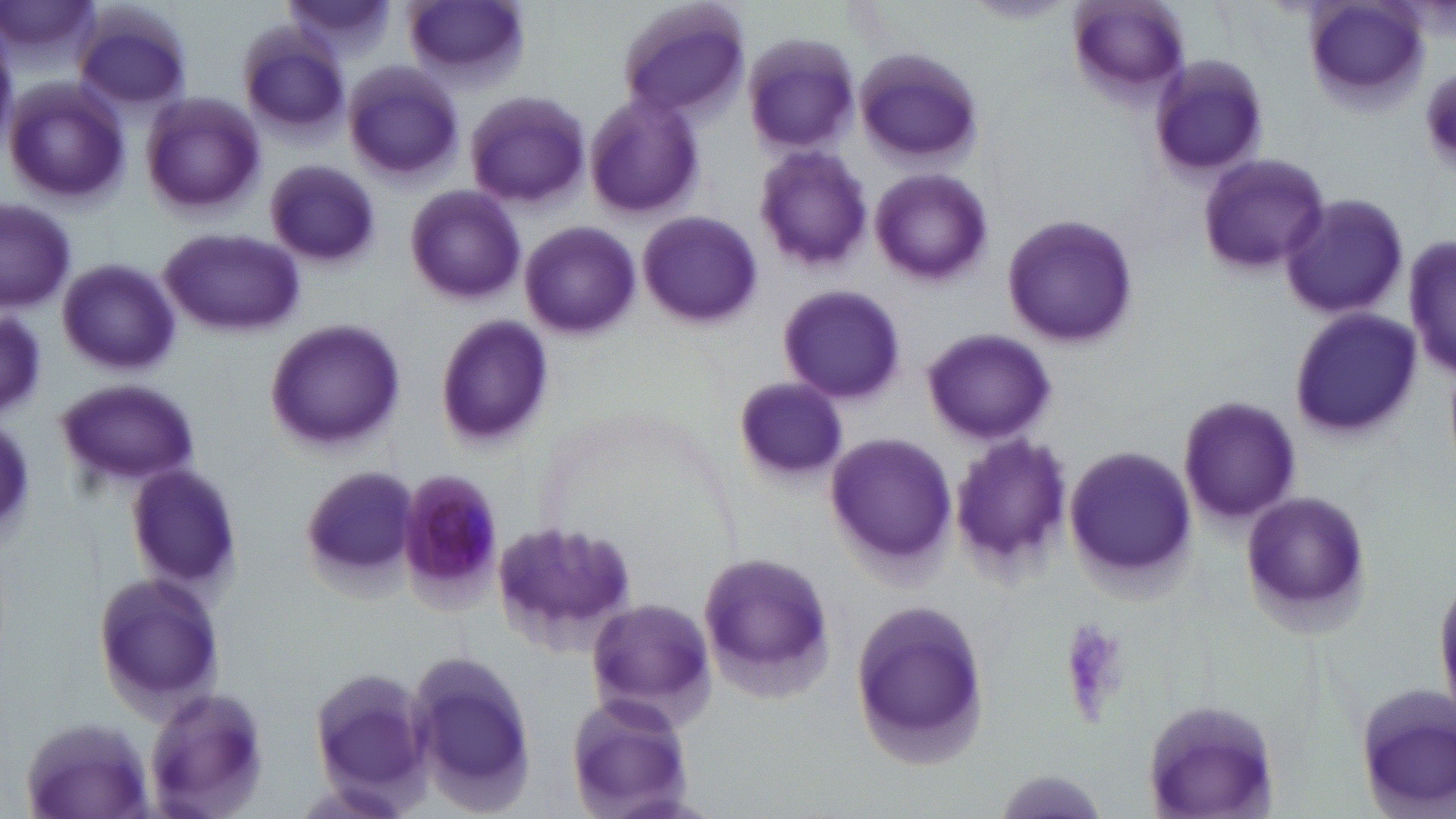 Approximate bounding boxes as named x1/y1/x2/y2 corners in pixels. Uninfected red blood cell locations: (x1=283, y1=0, x2=394, y2=60), (x1=404, y1=0, x2=526, y2=93), (x1=614, y1=0, x2=753, y2=121), (x1=967, y1=1, x2=1070, y2=24), (x1=1064, y1=1, x2=1193, y2=109), (x1=1299, y1=2, x2=1430, y2=113), (x1=74, y1=6, x2=192, y2=114), (x1=237, y1=24, x2=352, y2=139), (x1=741, y1=33, x2=863, y2=157), (x1=851, y1=46, x2=985, y2=169), (x1=1146, y1=54, x2=1270, y2=183), (x1=343, y1=63, x2=464, y2=183), (x1=5, y1=78, x2=130, y2=206), (x1=584, y1=89, x2=704, y2=221), (x1=463, y1=90, x2=591, y2=212), (x1=141, y1=91, x2=265, y2=218), (x1=751, y1=145, x2=874, y2=273), (x1=1196, y1=153, x2=1333, y2=279), (x1=266, y1=159, x2=379, y2=269), (x1=870, y1=169, x2=993, y2=286), (x1=404, y1=182, x2=524, y2=305), (x1=1276, y1=195, x2=1411, y2=320), (x1=1, y1=198, x2=76, y2=312), (x1=636, y1=211, x2=763, y2=330), (x1=1001, y1=212, x2=1138, y2=351), (x1=518, y1=220, x2=643, y2=341), (x1=160, y1=228, x2=304, y2=338), (x1=1408, y1=229, x2=1455, y2=384), (x1=57, y1=260, x2=181, y2=375), (x1=777, y1=286, x2=906, y2=406), (x1=1285, y1=308, x2=1423, y2=443), (x1=1, y1=309, x2=48, y2=413), (x1=435, y1=317, x2=554, y2=449), (x1=265, y1=318, x2=406, y2=452), (x1=921, y1=327, x2=1056, y2=445), (x1=58, y1=379, x2=203, y2=492), (x1=731, y1=379, x2=849, y2=481), (x1=1177, y1=393, x2=1302, y2=524), (x1=0, y1=411, x2=34, y2=544), (x1=825, y1=431, x2=955, y2=574), (x1=946, y1=433, x2=1072, y2=580), (x1=1064, y1=442, x2=1199, y2=589), (x1=125, y1=464, x2=246, y2=590), (x1=1237, y1=491, x2=1374, y2=634), (x1=490, y1=512, x2=639, y2=652), (x1=699, y1=548, x2=836, y2=699), (x1=91, y1=568, x2=226, y2=713), (x1=1431, y1=575, x2=1456, y2=706), (x1=585, y1=598, x2=718, y2=724), (x1=849, y1=598, x2=988, y2=768), (x1=396, y1=651, x2=542, y2=808), (x1=312, y1=667, x2=436, y2=794), (x1=142, y1=685, x2=272, y2=819), (x1=1352, y1=685, x2=1456, y2=813), (x1=565, y1=694, x2=694, y2=817), (x1=1140, y1=697, x2=1281, y2=819), (x1=17, y1=716, x2=156, y2=819), (x1=983, y1=769, x2=1118, y2=819). Plasmodium malariae-infected red blood cell locations: (x1=400, y1=467, x2=503, y2=605). Platelet locations: (x1=1058, y1=622, x2=1133, y2=720). Slide-level diagnosis: Plasmodium malariae. Image is 1456×819 pixels. 1000x magnification. Light microscopy. May-Grünwald-Giemsa stain. Thin blood smear. Single field of view.